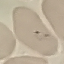
{
  "result": "malaria parasites identified",
  "image_type": "cell patch, automatically extracted from a larger field of view and resized to 64 × 64 pixels",
  "capture": "smartphone through the microscope eyepiece",
  "stain": "Giemsa",
  "preparation": "thin blood smear"
}